Report the malaria status.
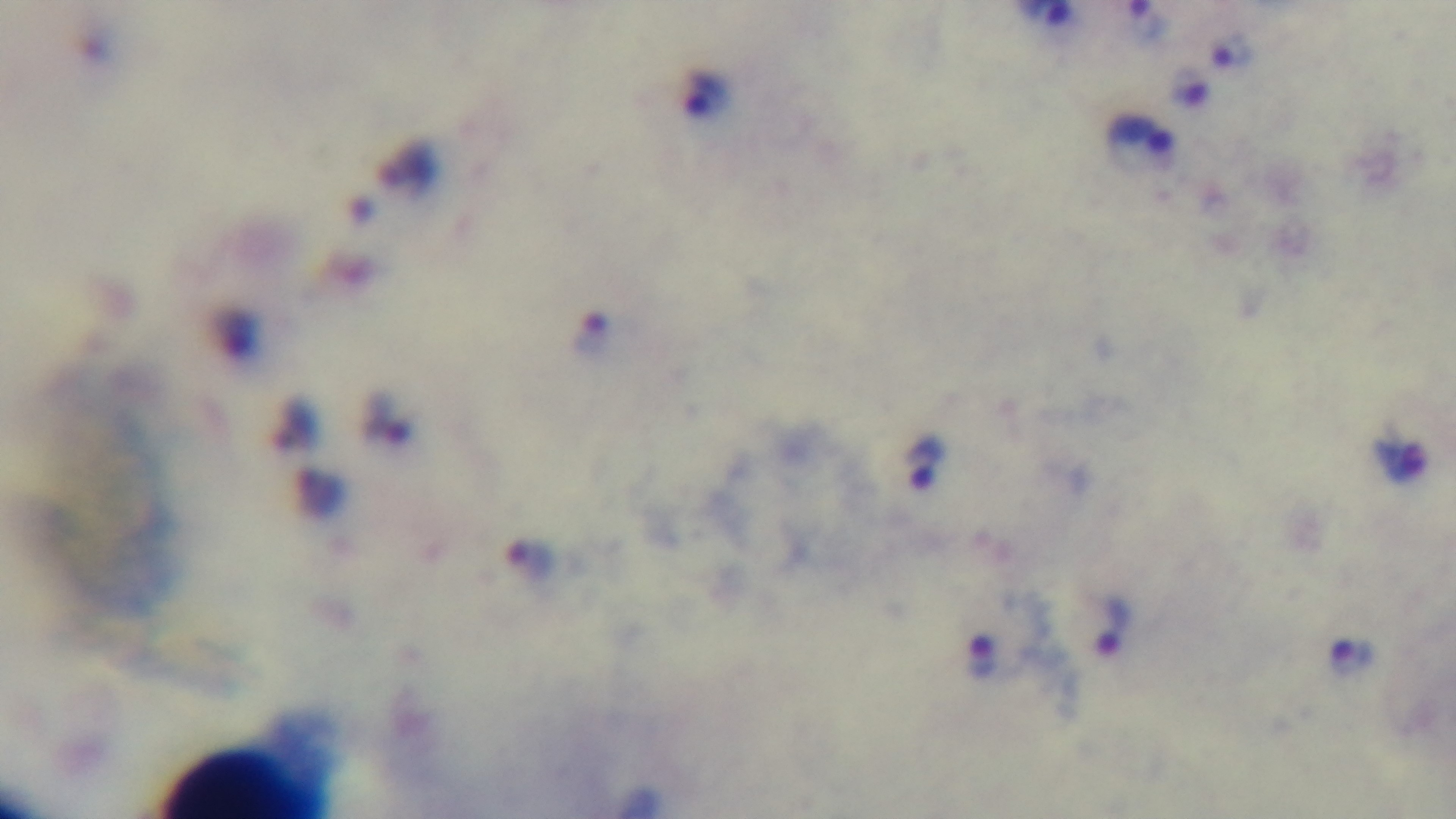
Infected.

Light microscopy. Preparation: thick blood film. 100x oil-immersion objective. Giemsa-stained. Single field of view. Mounted 4K digital camera.